State which cell type is depicted.
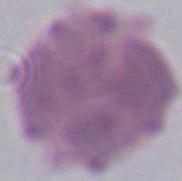

An erythrocyte.

Summary:
  - Modality: micrograph
  - Magnification: 1000x